Assess this cell for malaria.
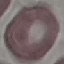
It is uninfected.

image_type: cell patch, automatically extracted from a larger field of view and resized to 64 × 64 pixels
capture: smartphone through the microscope eyepiece
preparation: thin blood film
stain: Giemsa